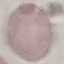 Result: negative for malaria parasites. Giemsa-stained preparation. Cell patch, automatically extracted from a larger field of view and resized to 64 × 64 pixels. Thin blood smear. Acquired by smartphone through the microscope eyepiece.